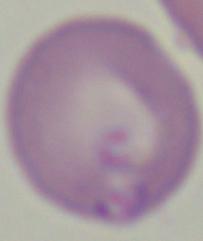

identification = Babesia
modality = photomicrograph
magnification = 1000x